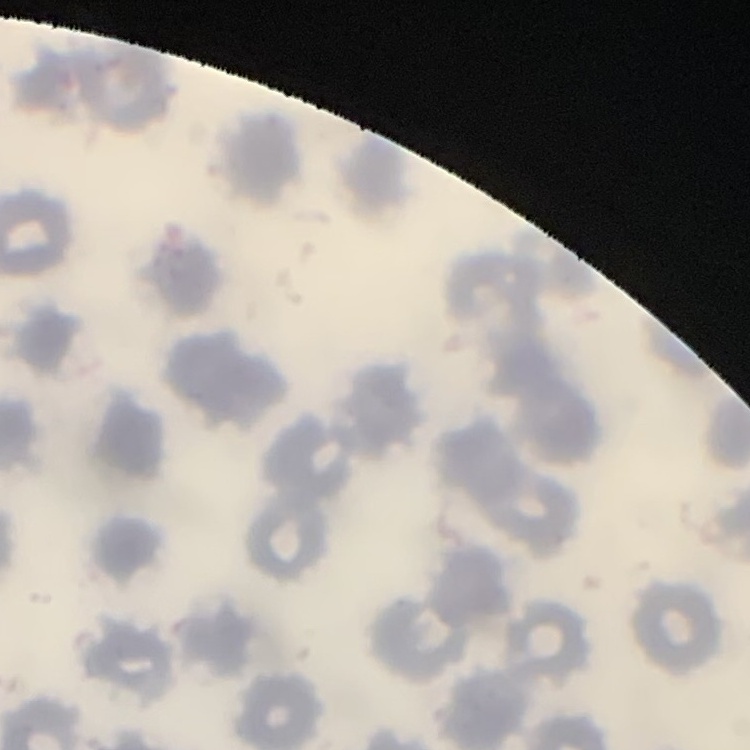
Summary:
  - Red blood cell morphology: no rouleaux formation
  - Stain: Field's or Giemsa
  - Image type: square crop of a larger photomicrograph
  - Preparation: thin peripheral smear